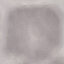 Result: negative for malaria parasites. Automatically extracted cell patch, resized to 64 × 64 pixels. Photographed with a smartphone camera at the microscope eyepiece. Thin blood smear. Giemsa stain.